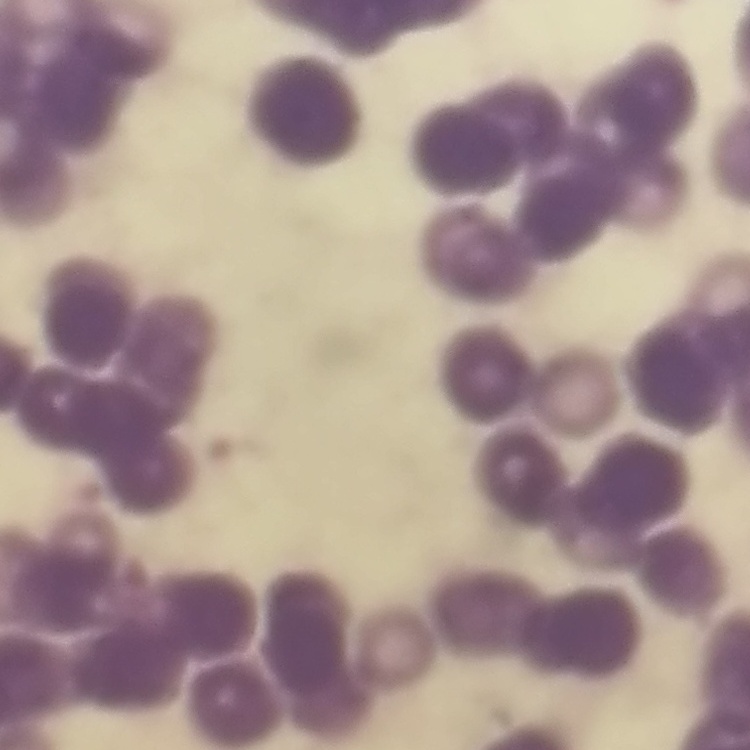
Summary:
  - Red blood cell morphology: rouleaux formation
  - Stain: Field's or Giemsa
  - Preparation: thin peripheral smear
  - Image type: one tile cut from a larger photomicrograph